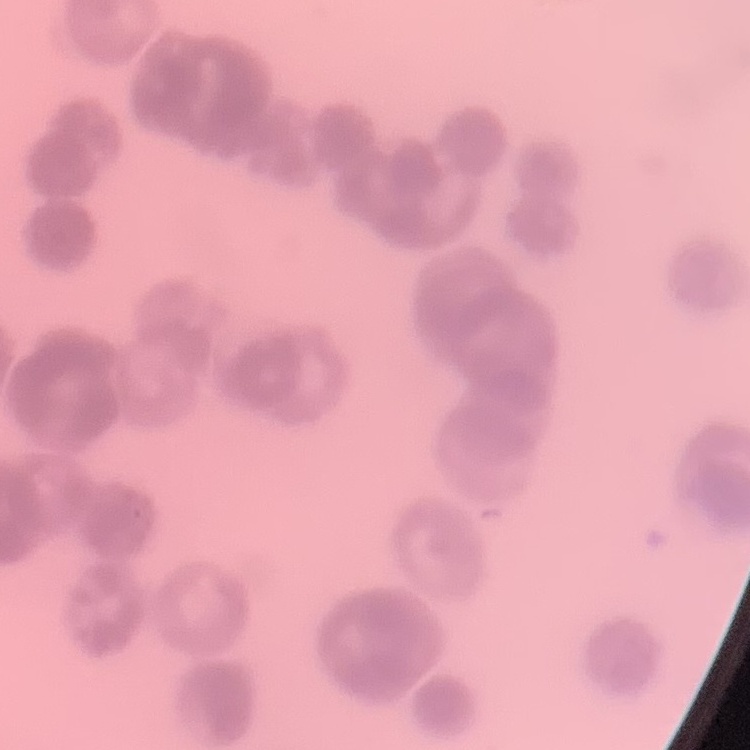
Summary:
  - Erythrocyte morphology: rouleaux formation
  - Preparation: thin blood film
  - Stain: Field's or Giemsa
  - Image type: one tile cut from a larger photomicrograph